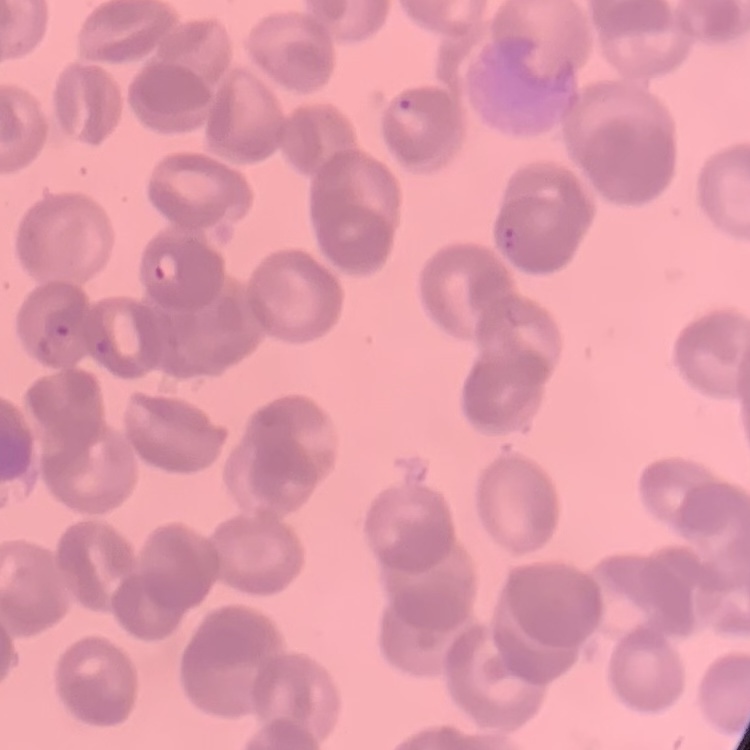

Summary:
  - Red blood cell morphology: rouleaux formation
  - Image type: square crop of a larger photomicrograph
  - Preparation: thin blood smear
  - Stain: Field's or Giemsa